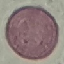

Summary:
  - Malaria status: uninfected
  - Capture: smartphone through the microscope eyepiece
  - Preparation: thin blood film
  - Stain: Giemsa
  - Image type: cell patch, automatically extracted from a larger field of view and resized to 64 × 64 pixels